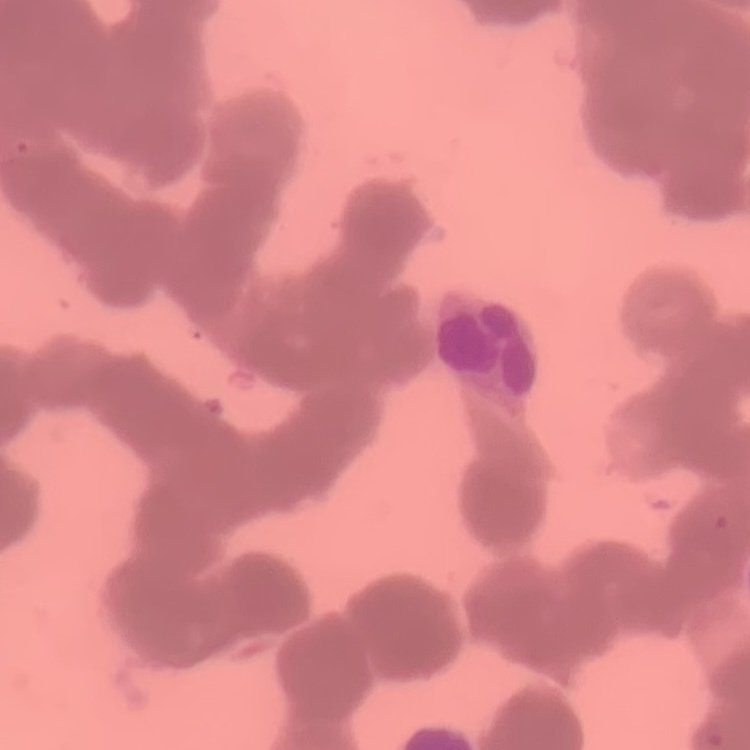
Summary:
  - Erythrocyte morphology: rouleaux formation
  - Stain: Field's or Giemsa
  - Preparation: thin blood film
  - Image type: one tile cut from a larger photomicrograph